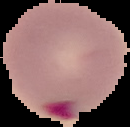

Summary:
  - Image size: 130×127 pixels
  - Image type: segmented cell region on a black background
  - Result: Plasmodium parasites detected
  - Preparation: thin blood film